Name the cell type shown.
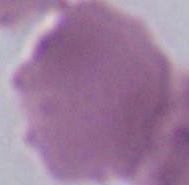
This is an erythrocyte.

Summary:
  - Modality: photomicrograph
  - Magnification: 1000x